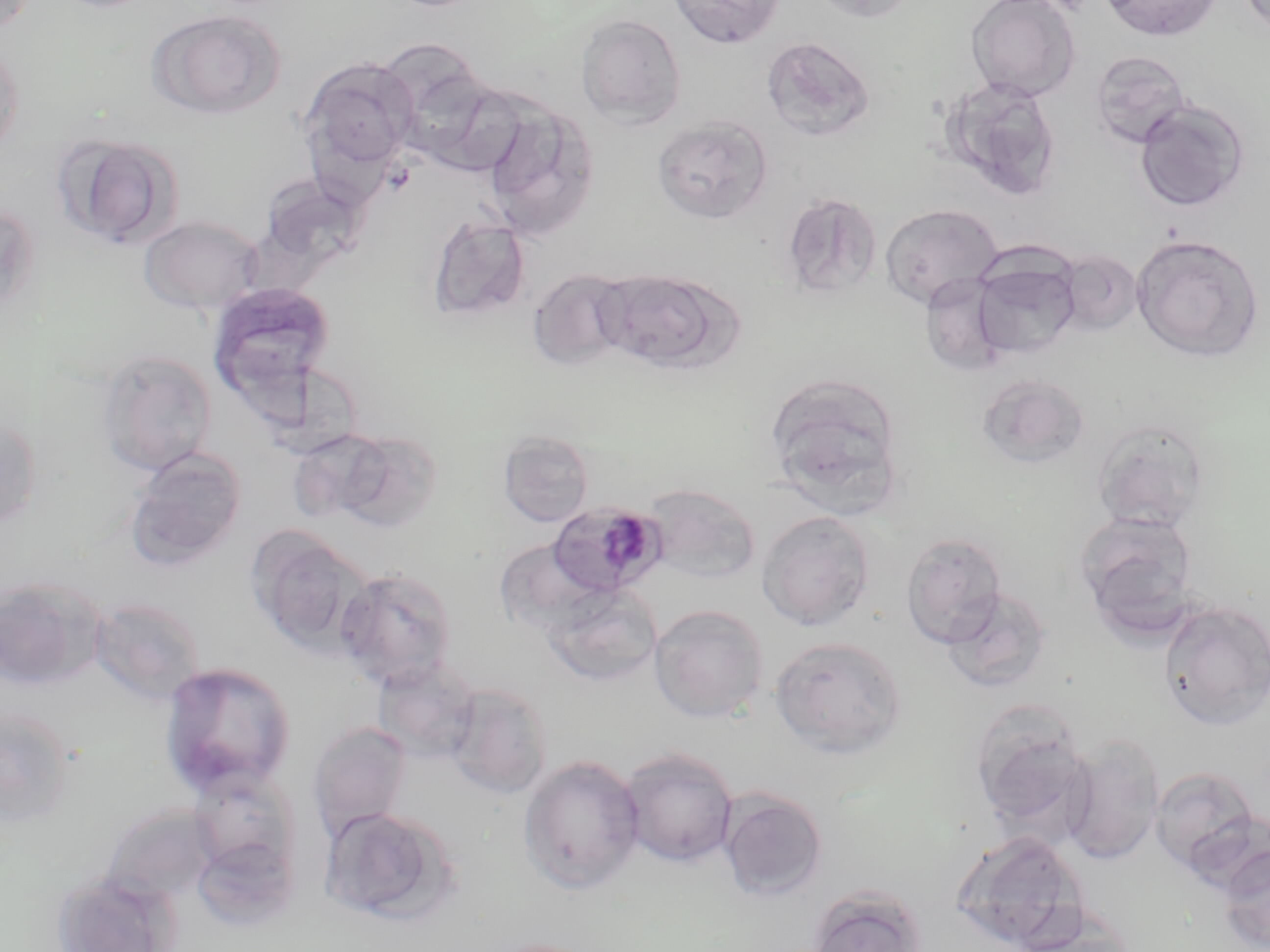

slide-level diagnosis = Plasmodium malariae
stain = May-Grünwald-Giemsa
modality = optical microscopy
magnification = 1000x
Plasmodium malariae-infected red blood cell locations = approximate bounding boxes as named x1/y1/x2/y2 corners in pixels: (x1=547, y1=502, x2=668, y2=599)
uninfected red blood cell locations = approximate bounding boxes as named x1/y1/x2/y2 corners in pixels: (x1=667, y1=0, x2=785, y2=49), (x1=805, y1=0, x2=921, y2=23), (x1=965, y1=0, x2=1081, y2=101), (x1=1099, y1=0, x2=1223, y2=42), (x1=0, y1=1, x2=40, y2=34), (x1=146, y1=8, x2=286, y2=119), (x1=575, y1=13, x2=686, y2=127), (x1=761, y1=37, x2=876, y2=144), (x1=0, y1=38, x2=24, y2=161), (x1=1090, y1=50, x2=1192, y2=149), (x1=300, y1=58, x2=418, y2=174), (x1=409, y1=71, x2=528, y2=177), (x1=941, y1=77, x2=1063, y2=203), (x1=1134, y1=99, x2=1249, y2=212), (x1=480, y1=100, x2=599, y2=240), (x1=652, y1=116, x2=772, y2=223), (x1=51, y1=132, x2=184, y2=250), (x1=259, y1=174, x2=370, y2=271), (x1=780, y1=193, x2=882, y2=300), (x1=0, y1=203, x2=41, y2=318), (x1=879, y1=203, x2=1004, y2=309), (x1=139, y1=214, x2=263, y2=313), (x1=427, y1=215, x2=530, y2=322), (x1=1131, y1=233, x2=1265, y2=362), (x1=1054, y1=249, x2=1143, y2=336), (x1=968, y1=255, x2=1081, y2=361), (x1=527, y1=268, x2=634, y2=371), (x1=596, y1=268, x2=736, y2=374), (x1=206, y1=282, x2=337, y2=407), (x1=97, y1=348, x2=218, y2=477), (x1=269, y1=365, x2=371, y2=461), (x1=976, y1=373, x2=1091, y2=469), (x1=765, y1=376, x2=905, y2=513), (x1=0, y1=413, x2=42, y2=532), (x1=1092, y1=418, x2=1213, y2=533), (x1=498, y1=429, x2=594, y2=527), (x1=295, y1=438, x2=394, y2=527), (x1=346, y1=438, x2=446, y2=534), (x1=124, y1=447, x2=246, y2=572), (x1=641, y1=483, x2=761, y2=583), (x1=756, y1=510, x2=877, y2=631), (x1=1074, y1=510, x2=1199, y2=635), (x1=248, y1=528, x2=375, y2=656), (x1=900, y1=532, x2=1008, y2=648), (x1=494, y1=540, x2=606, y2=636), (x1=335, y1=566, x2=457, y2=690), (x1=0, y1=576, x2=106, y2=691), (x1=542, y1=584, x2=663, y2=687), (x1=941, y1=587, x2=1053, y2=693), (x1=88, y1=597, x2=207, y2=705), (x1=1158, y1=599, x2=1270, y2=730), (x1=649, y1=603, x2=769, y2=723), (x1=770, y1=635, x2=907, y2=758), (x1=371, y1=658, x2=481, y2=763), (x1=158, y1=660, x2=296, y2=797), (x1=446, y1=682, x2=554, y2=799), (x1=0, y1=705, x2=76, y2=827), (x1=968, y1=707, x2=1096, y2=839), (x1=308, y1=720, x2=413, y2=837), (x1=1063, y1=734, x2=1166, y2=865), (x1=618, y1=747, x2=739, y2=868), (x1=518, y1=755, x2=646, y2=894), (x1=1149, y1=766, x2=1263, y2=873), (x1=186, y1=767, x2=302, y2=886), (x1=718, y1=789, x2=827, y2=902), (x1=100, y1=804, x2=219, y2=905), (x1=319, y1=806, x2=459, y2=924), (x1=190, y1=825, x2=299, y2=931), (x1=950, y1=830, x2=1086, y2=951), (x1=1218, y1=844, x2=1270, y2=952), (x1=50, y1=871, x2=180, y2=952), (x1=805, y1=884, x2=928, y2=952)
image size = 1270×952 pixels
preparation = thin blood smear
field of view = one of a larger specimen